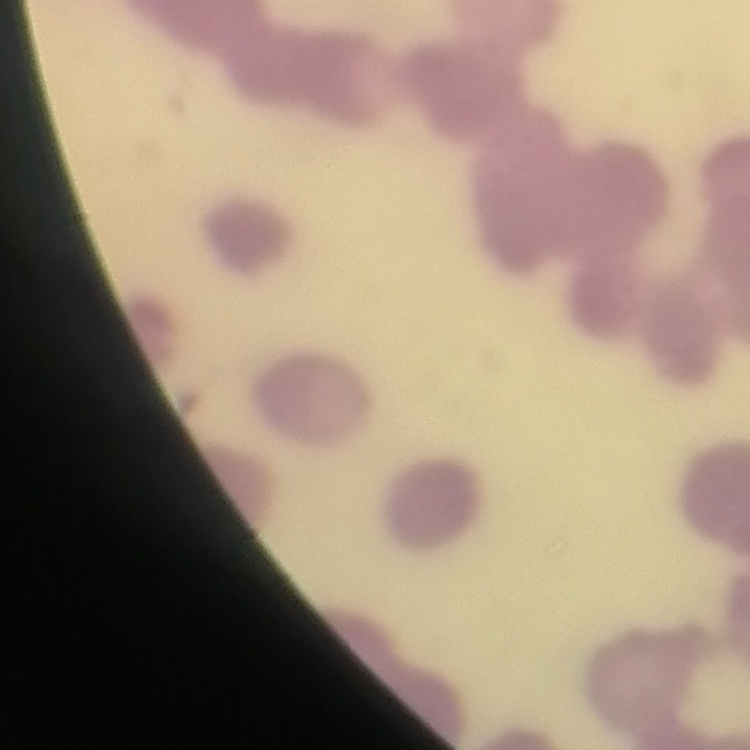

The red blood cells exhibit rouleaux formation. Stained with either Field's or Giemsa. Square crop of a larger photomicrograph. Thin blood smear.